Point out each Plasmodium parasite.
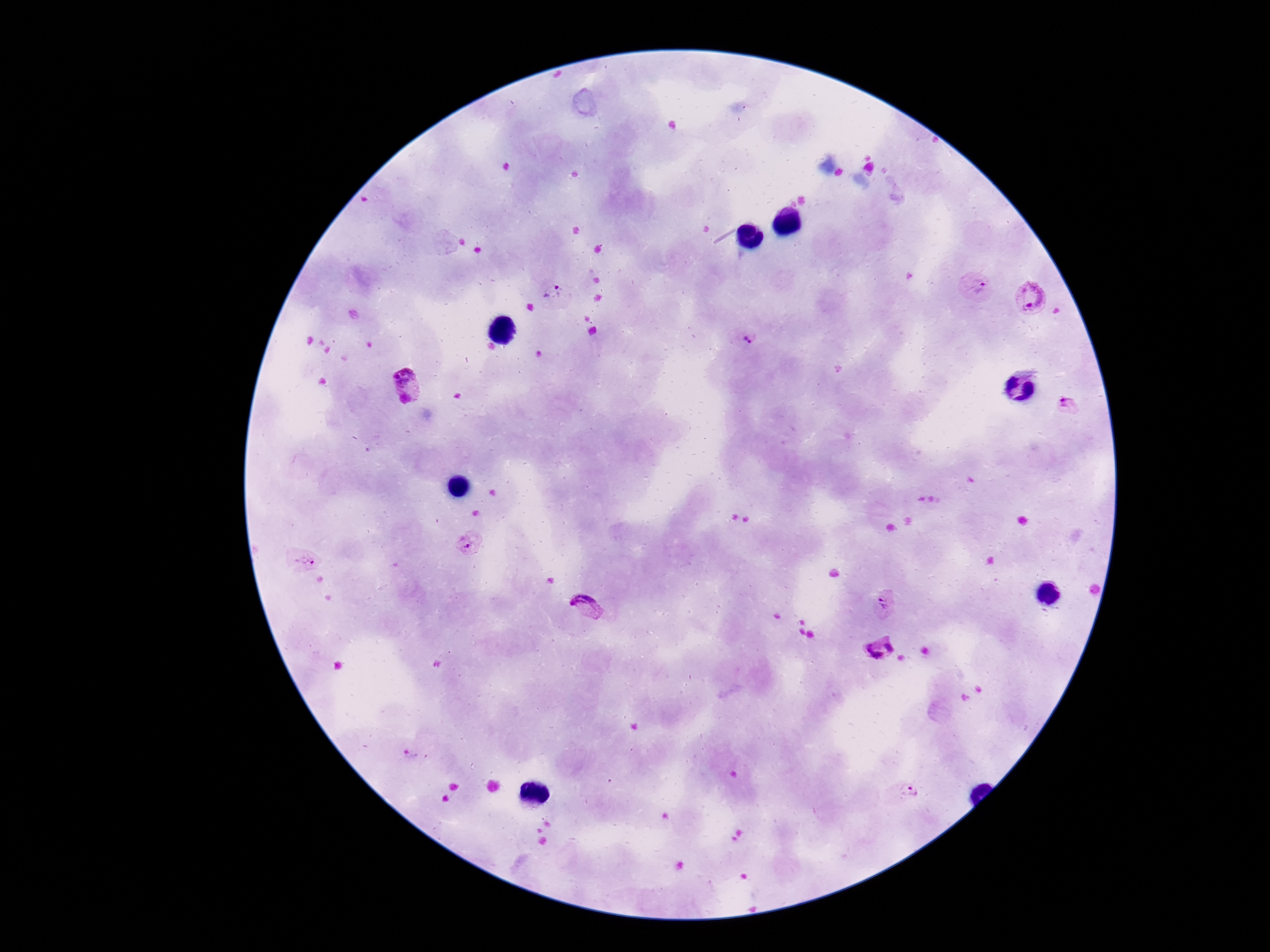
Approximate centers as {x, y} in pixels.
Plasmodium parasites: {976, 289}, {555, 293}, {1032, 298}, {744, 339}, {406, 377}, {1069, 406}, {471, 545}, {303, 561}, {886, 601}, {585, 609}, {881, 649}, {910, 792}.

{
  "magnification": "100x",
  "stain": "Giemsa",
  "capture": "smartphone camera through the microscope eyepiece",
  "patient_malaria_status": "positive",
  "image_size": "1270×952 pixels",
  "preparation": "thick peripheral-blood smear",
  "field_of_view": "one from this slide"
}